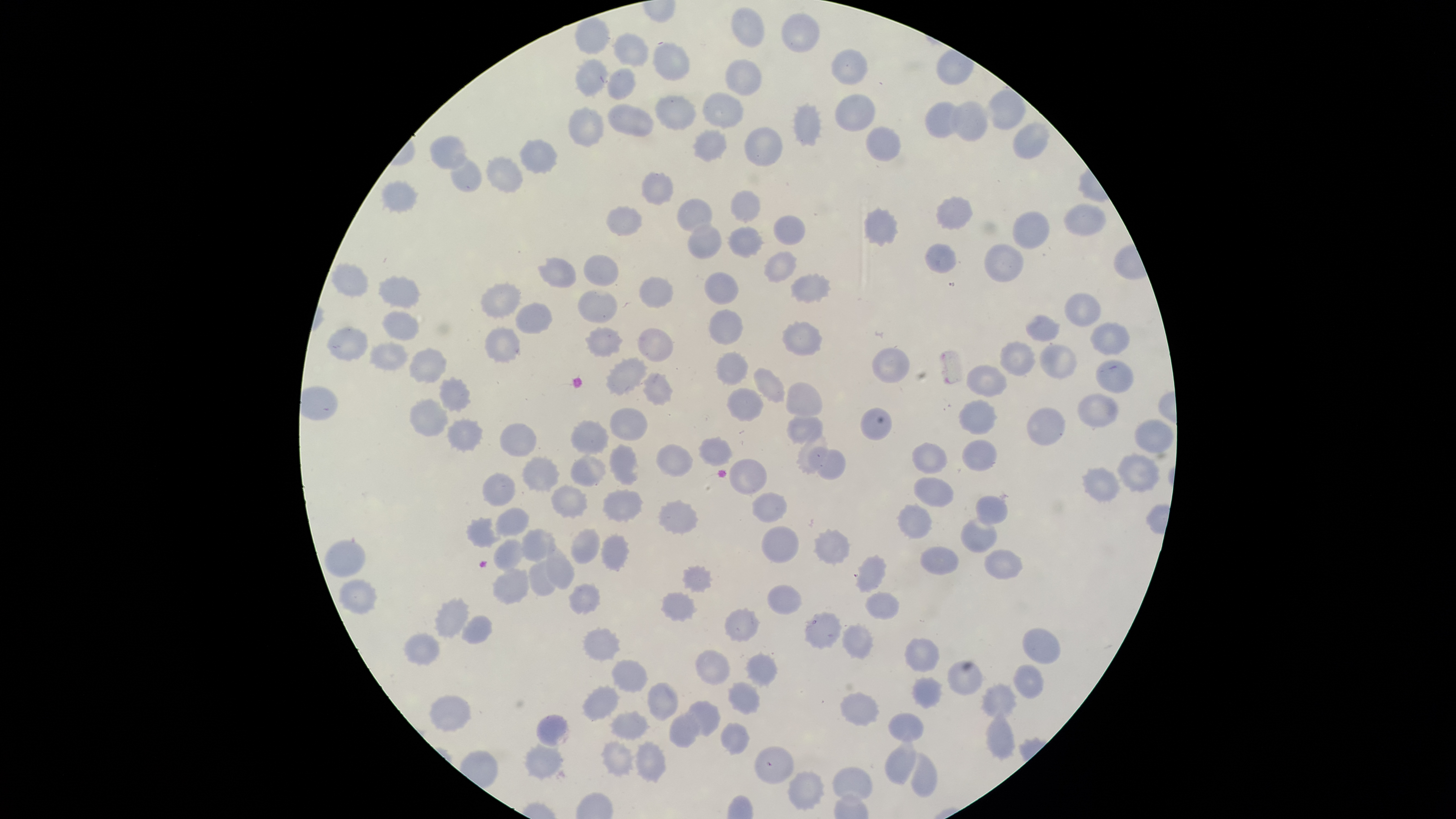

Approximate bounding boxes as (left, top, right, bottom) in pixels.
Summary:
  - Uninfected red blood cells: (732, 6, 763, 49), (782, 12, 820, 53), (576, 17, 610, 54), (613, 33, 648, 66), (653, 43, 690, 81), (831, 48, 868, 85), (575, 58, 607, 97), (724, 58, 762, 96), (608, 68, 637, 99), (987, 89, 1026, 129), (703, 91, 744, 129), (834, 94, 876, 132), (657, 95, 695, 130), (951, 100, 987, 142), (925, 101, 960, 139), (609, 103, 653, 137), (794, 104, 821, 147), (568, 106, 604, 148), (1012, 123, 1049, 161), (744, 127, 782, 168), (866, 127, 902, 162), (694, 129, 725, 162), (429, 134, 468, 171), (519, 139, 558, 174), (451, 153, 483, 193), (486, 157, 522, 193), (642, 171, 674, 205), (382, 180, 417, 213), (730, 191, 761, 221), (935, 197, 973, 231), (677, 199, 713, 232), (1066, 203, 1106, 238), (606, 206, 642, 237), (864, 209, 897, 246), (1014, 212, 1050, 251), (773, 215, 805, 247), (689, 224, 722, 259), (728, 226, 764, 259), (926, 243, 957, 275), (984, 245, 1023, 283), (765, 252, 796, 282), (584, 254, 620, 286), (539, 259, 576, 287), (333, 263, 369, 295), (705, 272, 738, 305), (791, 274, 830, 303), (380, 277, 420, 309), (640, 277, 674, 310), (481, 284, 520, 317), (578, 290, 618, 322), (1065, 294, 1102, 327), (515, 303, 553, 333), (709, 310, 742, 345), (382, 312, 419, 341), (1026, 315, 1059, 342), (782, 321, 821, 357), (1091, 324, 1130, 355), (328, 326, 367, 361), (586, 327, 622, 355), (486, 328, 520, 362), (639, 329, 673, 363), (1002, 341, 1036, 377), (370, 344, 406, 372), (1039, 345, 1077, 379), (410, 347, 446, 383), (872, 348, 910, 384), (716, 352, 748, 386), (607, 356, 646, 395), (1096, 359, 1134, 393), (754, 366, 785, 403), (965, 366, 1007, 396), (644, 372, 672, 406), (440, 377, 472, 412), (786, 383, 822, 416), (727, 388, 763, 421), (1078, 393, 1118, 428), (410, 399, 447, 436), (959, 400, 996, 435), (610, 407, 649, 440), (1027, 407, 1065, 447), (861, 408, 892, 441), (786, 413, 823, 443), (448, 418, 482, 450), (1134, 419, 1173, 453), (570, 420, 608, 456), (499, 421, 536, 457), (700, 436, 733, 465), (962, 440, 997, 472), (913, 442, 948, 474), (657, 443, 693, 477), (610, 445, 639, 484), (808, 446, 846, 479), (1116, 453, 1161, 491), (570, 455, 605, 486), (523, 456, 560, 491), (729, 458, 768, 492), (1082, 466, 1119, 503), (483, 471, 515, 507), (913, 478, 955, 507), (553, 485, 587, 518), (604, 489, 642, 521), (751, 492, 788, 522), (977, 496, 1007, 525), (659, 500, 699, 533), (898, 504, 931, 537), (495, 507, 529, 537), (466, 517, 501, 549), (961, 517, 997, 553), (763, 526, 798, 563), (570, 527, 599, 562), (520, 529, 555, 561), (815, 529, 850, 564), (602, 535, 629, 570), (493, 537, 525, 571), (325, 539, 366, 577), (548, 544, 575, 588), (921, 546, 958, 574), (985, 550, 1023, 580), (858, 554, 885, 592), (529, 560, 557, 596), (684, 566, 712, 591), (493, 569, 529, 604), (341, 577, 378, 613), (569, 583, 601, 614), (768, 585, 803, 615), (662, 592, 694, 621), (866, 592, 900, 618), (436, 596, 468, 637), (725, 609, 759, 641), (804, 611, 841, 648), (463, 616, 493, 643), (842, 623, 873, 660), (1023, 625, 1060, 664), (583, 627, 620, 662), (405, 634, 440, 665), (906, 637, 939, 673), (696, 650, 729, 686), (747, 653, 778, 686), (612, 660, 648, 692), (948, 660, 981, 696), (1014, 663, 1044, 698), (913, 677, 940, 709), (648, 680, 678, 720), (728, 681, 761, 715), (983, 684, 1016, 719), (583, 686, 618, 720), (841, 693, 880, 726), (431, 694, 471, 732), (686, 701, 721, 735), (612, 712, 648, 740), (669, 712, 701, 748), (987, 712, 1016, 758), (888, 713, 923, 741), (537, 714, 569, 746), (721, 723, 748, 754), (887, 734, 914, 783), (602, 742, 632, 777), (635, 742, 666, 782), (524, 744, 561, 778), (755, 746, 794, 784), (911, 752, 938, 798), (833, 767, 872, 801), (787, 770, 823, 808)
  - Field of view: single
  - Visible region: circular
  - Capture: smartphone photograph through the microscope eyepiece
  - Preparation: thin blood smear
  - Stain: Giemsa
  - Presence: no malaria parasites identified
  - Image size: 1456×819 pixels